Locate every blood parasite and identify its species.
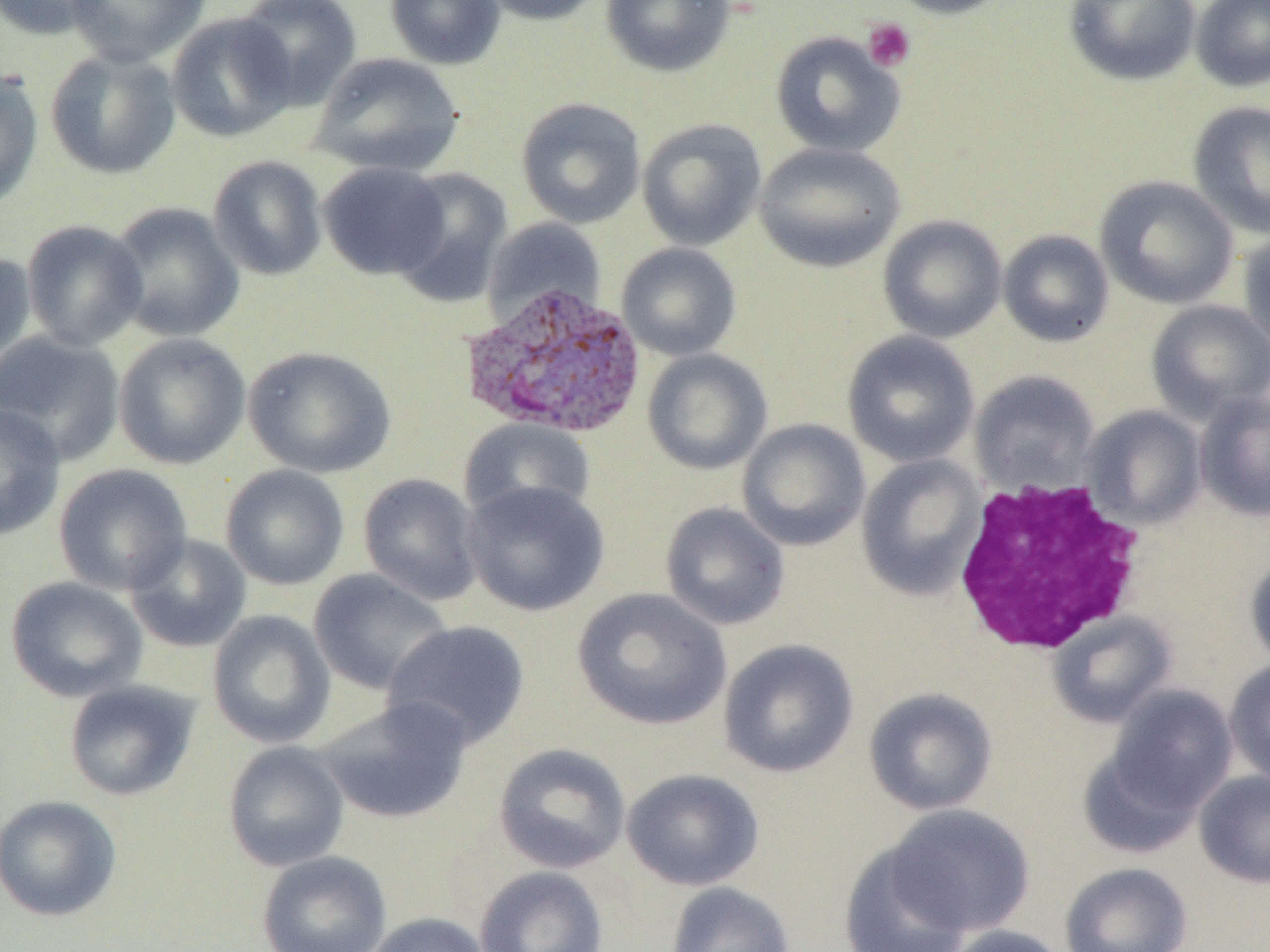

Approximate bounding boxes as named x1/y1/x2/y2 corners in pixels.
Plasmodium vivax-infected red blood cells: (x1=459, y1=281, x2=649, y2=438).
No Plasmodium falciparum, Plasmodium ovale, Plasmodium malariae, Babesia divergens, or Trypanosoma brucei observed.

Summary:
  - Platelet locations: (x1=863, y1=18, x2=916, y2=72)
  - Uninfected red blood cell locations: (x1=1, y1=0, x2=109, y2=41), (x1=65, y1=0, x2=210, y2=67), (x1=234, y1=0, x2=362, y2=111), (x1=384, y1=0, x2=506, y2=70), (x1=475, y1=0, x2=602, y2=26), (x1=601, y1=0, x2=737, y2=78), (x1=884, y1=0, x2=1015, y2=19), (x1=1064, y1=0, x2=1201, y2=87), (x1=1190, y1=0, x2=1270, y2=93), (x1=167, y1=13, x2=298, y2=143), (x1=770, y1=31, x2=906, y2=158), (x1=44, y1=48, x2=182, y2=180), (x1=311, y1=52, x2=465, y2=177), (x1=0, y1=68, x2=44, y2=212), (x1=515, y1=97, x2=646, y2=229), (x1=1187, y1=101, x2=1270, y2=239), (x1=637, y1=118, x2=767, y2=251), (x1=754, y1=141, x2=905, y2=273), (x1=208, y1=155, x2=327, y2=281), (x1=318, y1=161, x2=450, y2=280), (x1=390, y1=167, x2=513, y2=306), (x1=1095, y1=175, x2=1239, y2=309), (x1=107, y1=202, x2=245, y2=343), (x1=877, y1=215, x2=1008, y2=343), (x1=484, y1=217, x2=607, y2=325), (x1=21, y1=220, x2=149, y2=351), (x1=998, y1=229, x2=1114, y2=348), (x1=1238, y1=231, x2=1270, y2=361), (x1=616, y1=243, x2=742, y2=361), (x1=0, y1=250, x2=36, y2=375), (x1=1146, y1=300, x2=1270, y2=423), (x1=0, y1=330, x2=126, y2=468), (x1=842, y1=330, x2=980, y2=468), (x1=113, y1=332, x2=251, y2=470), (x1=243, y1=346, x2=396, y2=478), (x1=642, y1=348, x2=772, y2=475), (x1=969, y1=370, x2=1100, y2=494), (x1=1195, y1=390, x2=1270, y2=522), (x1=0, y1=402, x2=65, y2=542), (x1=1084, y1=406, x2=1207, y2=528), (x1=459, y1=418, x2=596, y2=523), (x1=737, y1=418, x2=871, y2=551), (x1=856, y1=454, x2=987, y2=600), (x1=53, y1=463, x2=193, y2=596), (x1=220, y1=464, x2=350, y2=591), (x1=358, y1=473, x2=484, y2=606), (x1=462, y1=479, x2=610, y2=616), (x1=660, y1=501, x2=790, y2=631), (x1=124, y1=533, x2=252, y2=653), (x1=1246, y1=554, x2=1270, y2=672), (x1=308, y1=569, x2=453, y2=695), (x1=5, y1=576, x2=148, y2=703), (x1=572, y1=587, x2=731, y2=730), (x1=207, y1=609, x2=336, y2=748), (x1=1048, y1=611, x2=1178, y2=728), (x1=382, y1=620, x2=531, y2=749), (x1=718, y1=638, x2=859, y2=778), (x1=1224, y1=659, x2=1270, y2=788), (x1=63, y1=680, x2=200, y2=801), (x1=1106, y1=684, x2=1238, y2=814), (x1=863, y1=686, x2=998, y2=816), (x1=315, y1=696, x2=473, y2=825), (x1=223, y1=741, x2=350, y2=872), (x1=493, y1=743, x2=631, y2=873), (x1=1077, y1=744, x2=1207, y2=858), (x1=621, y1=767, x2=765, y2=891), (x1=1194, y1=771, x2=1270, y2=888), (x1=0, y1=794, x2=122, y2=922), (x1=883, y1=804, x2=1036, y2=937), (x1=839, y1=842, x2=974, y2=952), (x1=256, y1=850, x2=392, y2=952), (x1=1059, y1=862, x2=1193, y2=952), (x1=474, y1=865, x2=608, y2=952), (x1=664, y1=881, x2=795, y2=952), (x1=363, y1=912, x2=493, y2=952), (x1=941, y1=924, x2=1072, y2=952)
  - White blood cell locations: (x1=952, y1=475, x2=1148, y2=656)
  - Slide-level diagnosis: Plasmodium vivax
  - Modality: light microscopy
  - Magnification: 1000x
  - Preparation: thin blood smear
  - Field of view: single
  - Image size: 1270×952 pixels